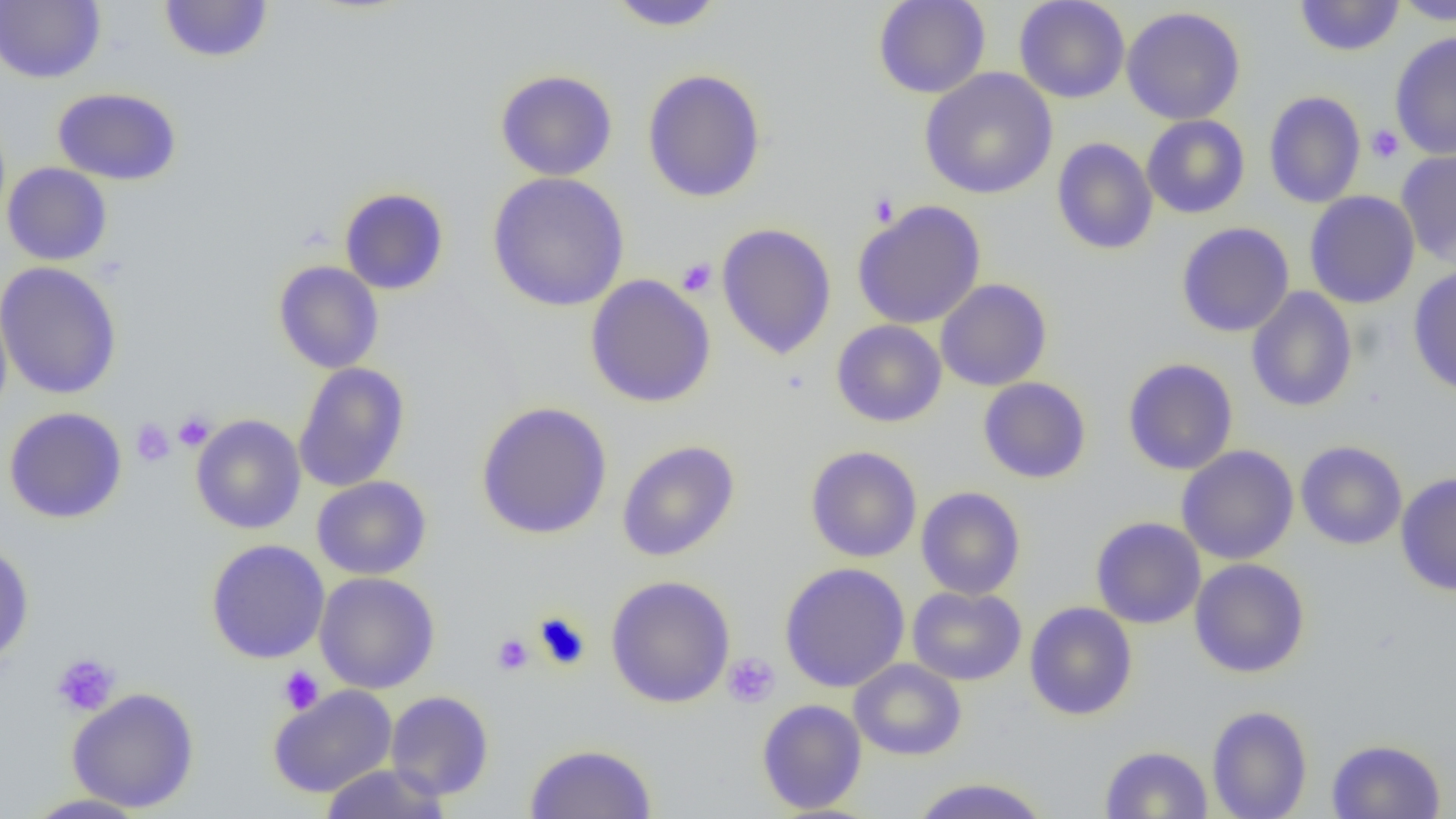
Summary:
  - Coordinate format: approximate bounding boxes as (x1,y1)-(x2,y2) corner pairs in pixels
  - Platelet locations: (1365,124)-(1404,164), (868,192)-(900,228), (677,258)-(717,297), (173,411)-(215,451), (130,418)-(175,467), (534,611)-(591,671), (492,633)-(534,676), (51,652)-(121,717), (722,652)-(780,708), (277,666)-(324,715)
  - Uninfected red blood cell locations: (158,0)-(274,64), (872,0)-(991,99), (1013,0)-(1130,103), (1294,0)-(1405,57), (1390,0)-(1456,25), (0,1)-(106,84), (607,1)-(728,31), (1121,6)-(1246,125), (1389,32)-(1456,160), (641,68)-(767,203), (920,68)-(1058,200), (494,69)-(618,182), (52,87)-(182,186), (1264,91)-(1366,208), (1141,114)-(1250,219), (1052,138)-(1158,255), (1395,148)-(1456,267), (2,163)-(112,266), (486,172)-(631,312), (339,187)-(449,295), (1304,191)-(1420,308), (852,199)-(986,329), (716,222)-(837,359), (1176,222)-(1294,337), (273,260)-(384,373), (0,261)-(122,400), (1408,265)-(1456,397), (585,274)-(716,408), (936,279)-(1052,391), (1246,287)-(1358,413), (0,298)-(13,422), (831,320)-(946,428), (1123,358)-(1238,475), (293,362)-(410,493), (978,377)-(1091,484), (476,401)-(612,539), (3,407)-(127,524), (190,414)-(306,534), (616,440)-(739,562), (1295,440)-(1408,550), (805,445)-(922,563), (1176,445)-(1299,565), (1396,472)-(1456,596), (312,475)-(432,580), (915,486)-(1026,600), (1090,516)-(1206,629), (205,539)-(330,664), (0,541)-(34,667), (1189,558)-(1310,678), (779,562)-(910,693), (314,572)-(440,694), (605,575)-(735,708), (907,585)-(1026,686), (1024,602)-(1138,721), (849,658)-(967,761), (268,685)-(398,798), (67,687)-(200,813), (385,690)-(495,800), (756,698)-(867,814), (1206,705)-(1313,819), (1326,738)-(1446,818), (524,742)-(657,819), (1100,745)-(1213,818), (319,762)-(452,818), (908,777)-(1053,818), (21,793)-(153,818)
  - Slide-level diagnosis: no evidence of blood parasites
  - Preparation: thin blood film
  - Modality: optical microscopy
  - Magnification: 1000x
  - Image size: 1456×819 pixels
  - Field of view: one of a larger specimen